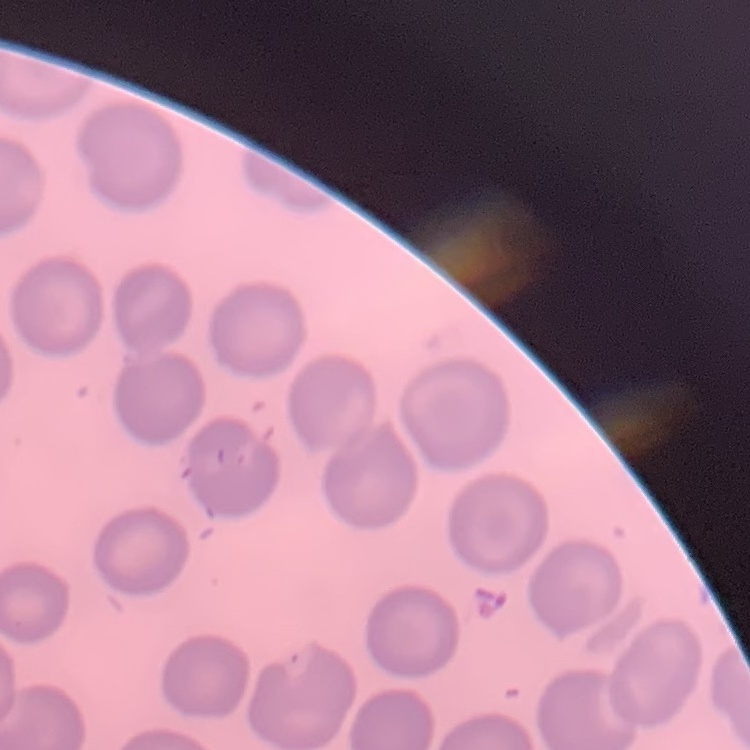

erythrocyte morphology = no rouleaux formation
image type = one tile cut from a larger photomicrograph
preparation = thin blood smear
stain = Field's or Giemsa